Locate and identify every blood parasite.
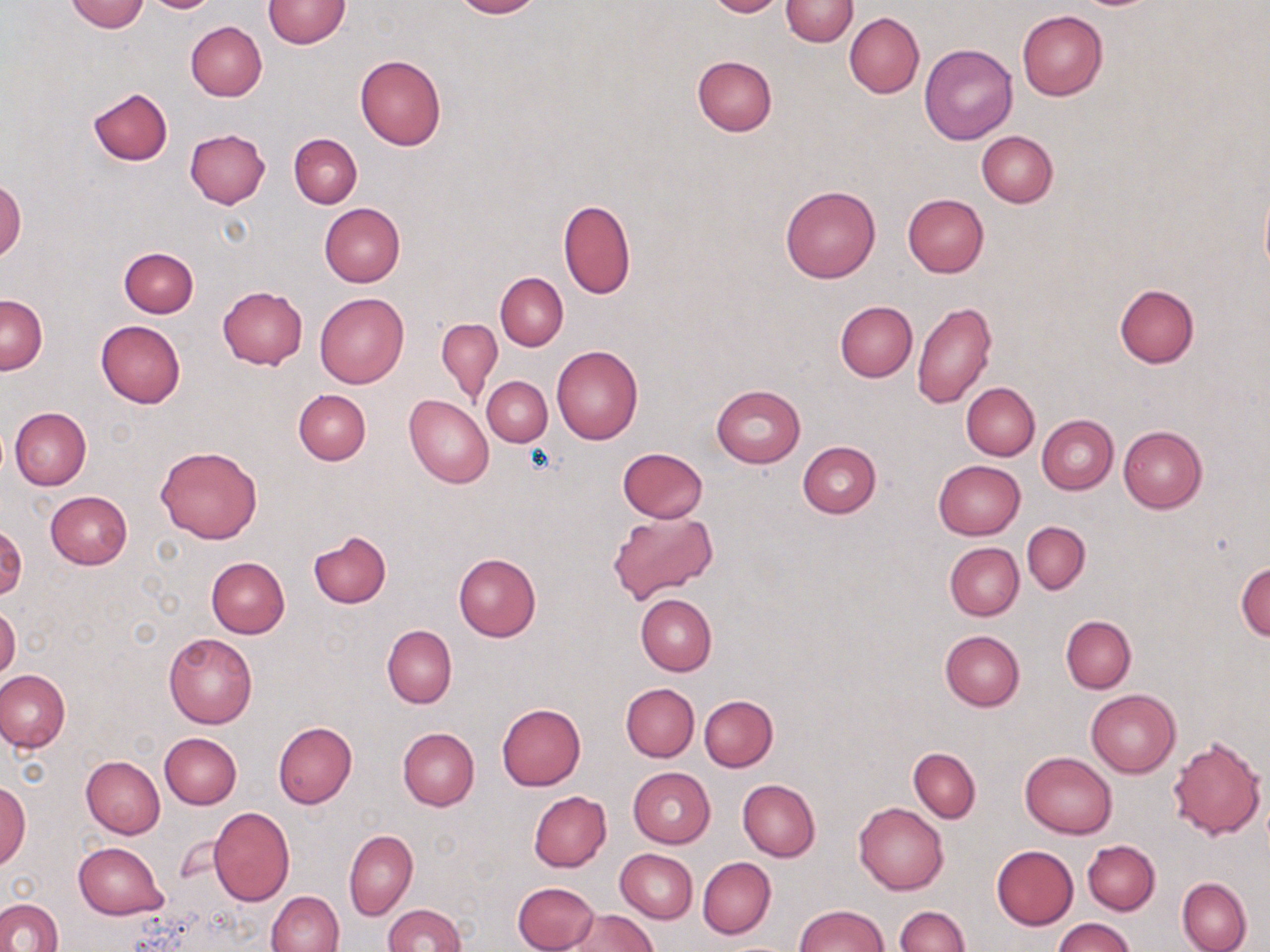
No blood parasites seen.

slide-level diagnosis = negative for blood parasites
stain = May-Grünwald-Giemsa
uninfected red blood cell locations = approximate bounding boxes as (x1,y1)-(x2,y2) corner pairs in pixels: (66,0)-(150,32), (146,0)-(216,13), (450,0)-(543,18), (704,0)-(787,18), (781,0)-(857,46), (264,1)-(348,48), (1017,11)-(1108,100), (844,13)-(924,98), (185,21)-(266,100), (919,44)-(1018,144), (354,54)-(447,150), (692,56)-(776,137), (88,87)-(172,166), (184,129)-(270,208), (977,131)-(1058,207), (289,133)-(362,208), (0,176)-(26,262), (1259,183)-(1270,282), (780,184)-(881,283), (902,193)-(989,278), (558,200)-(636,299), (319,203)-(405,287), (119,247)-(198,317), (496,273)-(568,350), (1114,285)-(1198,368), (218,286)-(308,369), (315,293)-(408,388), (0,295)-(47,375), (911,300)-(997,409), (835,301)-(917,382), (437,319)-(502,403), (95,320)-(186,408), (552,345)-(643,445), (482,376)-(553,446), (962,383)-(1040,460), (711,384)-(805,467), (293,388)-(371,465), (404,395)-(494,488), (10,407)-(92,489), (1037,415)-(1118,495), (1118,426)-(1207,513), (798,441)-(881,518), (155,444)-(263,545), (617,447)-(709,523), (933,460)-(1026,540), (45,491)-(133,569), (607,511)-(719,606), (1022,521)-(1090,596), (0,522)-(26,602), (309,530)-(391,606), (944,543)-(1024,621), (453,553)-(541,642), (207,557)-(290,637), (1236,562)-(1270,639), (636,593)-(716,675), (0,605)-(20,681), (1061,616)-(1136,693), (382,625)-(456,708), (940,629)-(1024,711), (163,632)-(256,729), (0,669)-(70,751), (621,683)-(699,762), (1086,688)-(1181,778), (700,694)-(777,771), (496,703)-(586,789), (272,721)-(357,809), (398,727)-(479,810), (160,733)-(242,808), (1166,735)-(1266,840), (908,748)-(981,822), (1020,752)-(1115,839), (81,756)-(165,839), (627,767)-(715,848), (738,780)-(821,861), (0,781)-(30,870), (529,791)-(611,872), (854,803)-(948,895), (207,807)-(295,905), (344,829)-(417,920), (1082,840)-(1160,915), (73,842)-(169,919), (992,845)-(1078,929), (616,849)-(697,922), (698,856)-(775,939), (1177,877)-(1252,952), (513,881)-(600,952), (266,890)-(343,952), (0,899)-(63,952), (383,904)-(464,952), (793,904)-(888,952), (894,906)-(970,952), (569,909)-(657,952), (1052,917)-(1133,952)
magnification = 1000x
field of view = one of a larger specimen
preparation = thin blood film
modality = optical microscopy
image size = 1270×952 pixels